Assess this cell for malaria.
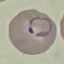

Parasitized.

Summary:
  - Stain: Giemsa
  - Preparation: thin blood smear
  - Image type: automatically extracted cell patch, resized to 64 × 64 pixels
  - Capture: smartphone through the microscope eyepiece